Outline each blood parasite and name the species.
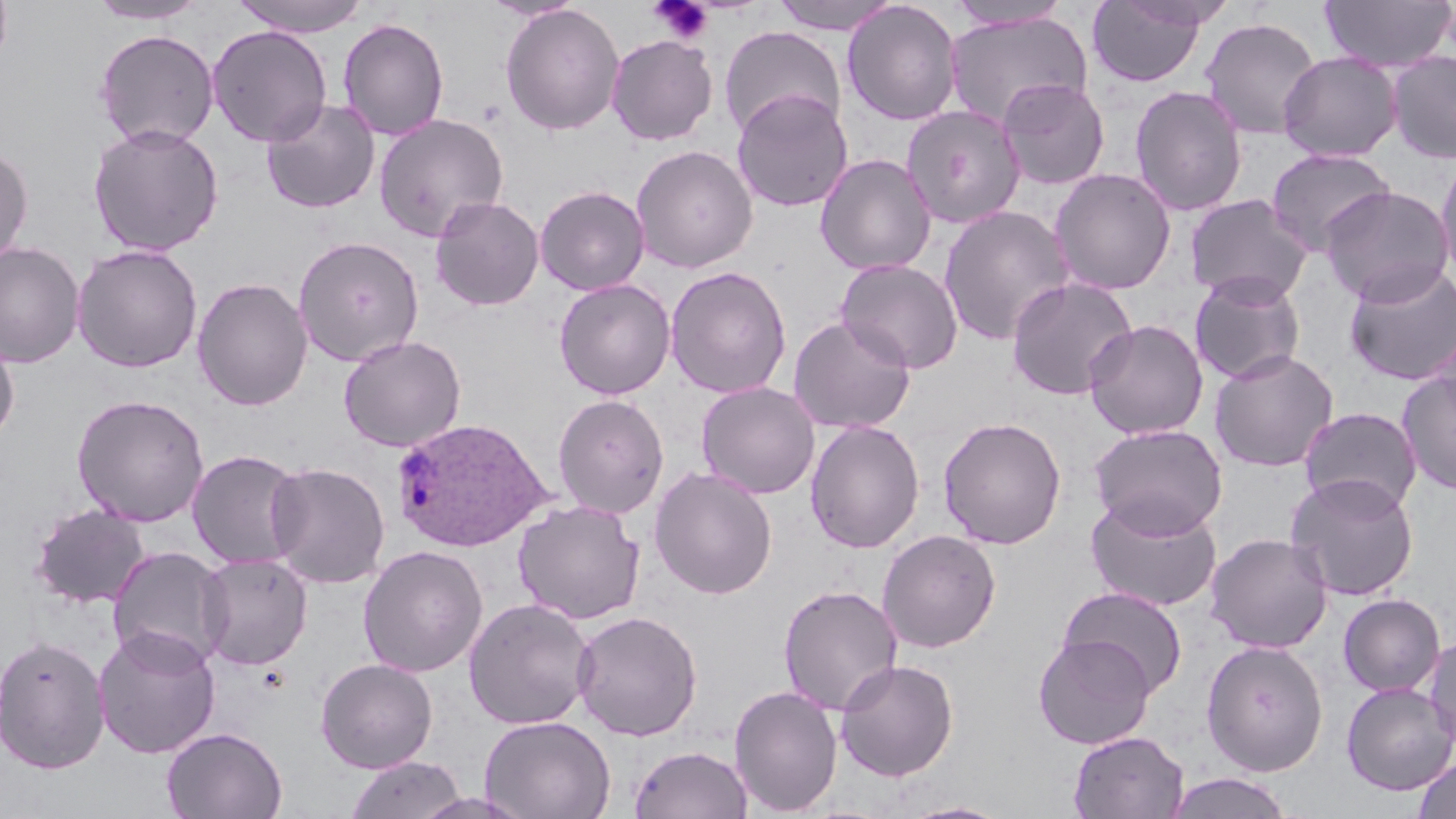

Approximate bounding boxes as [x1, y1, x2, y2] in pixels.
Plasmodium ovale-infected red blood cells: [391, 418, 552, 551].
No Plasmodium falciparum, Plasmodium malariae, Plasmodium vivax, Babesia divergens, or Trypanosoma brucei observed.

Summary:
  - Uninfected red blood cell locations: [87, 0, 208, 25], [230, 0, 371, 37], [480, 0, 587, 22], [769, 0, 904, 35], [1086, 0, 1210, 88], [842, 1, 963, 127], [946, 1, 1072, 31], [1319, 1, 1456, 72], [500, 4, 625, 136], [943, 11, 1093, 128], [1200, 17, 1322, 140], [338, 18, 449, 140], [207, 25, 332, 146], [719, 26, 846, 139], [94, 29, 219, 149], [606, 34, 718, 146], [1387, 50, 1456, 164], [1278, 51, 1403, 162], [996, 78, 1110, 190], [1129, 85, 1248, 217], [732, 89, 852, 212], [261, 98, 380, 214], [901, 105, 1027, 228], [373, 113, 509, 242], [88, 123, 224, 257], [0, 144, 33, 267], [631, 144, 758, 273], [1265, 147, 1395, 257], [1435, 153, 1456, 286], [815, 154, 937, 275], [1049, 168, 1177, 295], [535, 185, 649, 295], [1319, 185, 1454, 305], [1184, 193, 1313, 305], [430, 196, 544, 311], [938, 205, 1075, 346], [293, 236, 424, 366], [0, 242, 84, 368], [71, 244, 203, 373], [836, 258, 963, 374], [1343, 262, 1456, 386], [665, 266, 792, 399], [1189, 272, 1307, 385], [1005, 276, 1138, 401], [192, 277, 312, 411], [554, 278, 676, 400], [789, 315, 916, 434], [1083, 319, 1209, 440], [1432, 321, 1456, 434], [0, 332, 20, 448], [338, 335, 466, 452], [1209, 348, 1339, 472], [1396, 370, 1456, 495], [696, 382, 820, 499], [72, 393, 209, 527], [553, 393, 669, 518], [1299, 406, 1422, 516], [938, 416, 1067, 549], [805, 420, 925, 553], [1089, 423, 1228, 537], [187, 449, 306, 570], [265, 461, 390, 588], [648, 466, 778, 600], [1285, 472, 1420, 601], [1085, 494, 1223, 612], [512, 499, 646, 625], [30, 503, 150, 608], [877, 529, 1002, 653], [1204, 532, 1333, 654], [357, 545, 488, 677], [106, 546, 230, 670], [197, 552, 313, 671], [777, 584, 903, 716], [1057, 586, 1188, 698], [1338, 593, 1446, 697], [463, 597, 596, 731], [571, 610, 703, 741], [92, 625, 221, 759], [1424, 633, 1456, 753], [1033, 634, 1156, 749], [0, 635, 110, 774], [1201, 640, 1329, 776], [315, 658, 438, 773], [834, 659, 959, 782], [1341, 681, 1456, 795], [729, 684, 843, 816], [479, 715, 615, 819], [162, 726, 287, 818], [1069, 731, 1189, 818], [629, 745, 753, 819], [344, 755, 468, 818], [1413, 757, 1456, 819], [1164, 772, 1294, 818], [411, 792, 535, 819], [897, 800, 1013, 819]
  - Platelet locations: [648, 0, 714, 45]
  - Slide-level diagnosis: Plasmodium ovale
  - Magnification: 1000x
  - Stain: May-Grünwald-Giemsa
  - Modality: light microscopy
  - Field of view: single
  - Image size: 1456×819 pixels
  - Preparation: thin blood film